Describe the morphology of the erythrocytes.
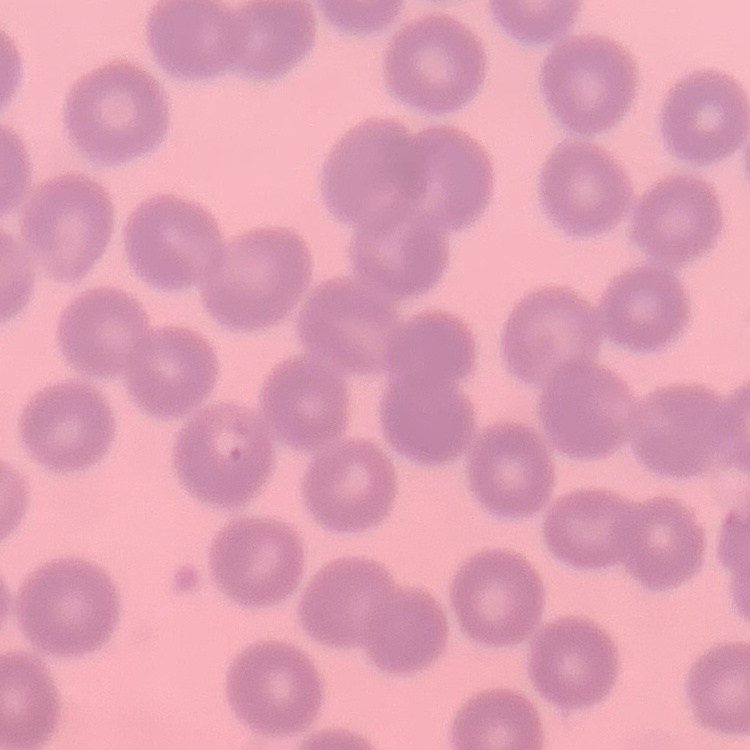

They show no rouleaux formation.

preparation = thin blood smear
stain = Field's or Giemsa
image type = one tile cut from a larger photomicrograph